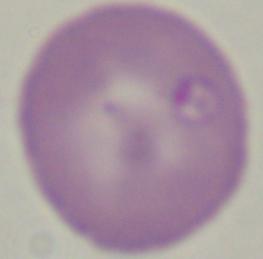

Captured at 1000x magnification. A Babesia parasite is seen. Photomicrograph.